Classify this cell by malaria status.
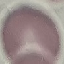

It is uninfected.

Photographed with a smartphone camera at the microscope eyepiece. Cell patch, automatically extracted from a larger field of view and resized to 64 × 64 pixels. Thin blood smear. Giemsa stain.